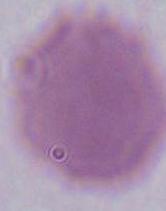
Captured at 1000x magnification. An erythrocyte is seen. Micrograph.